State which parasite is depicted.
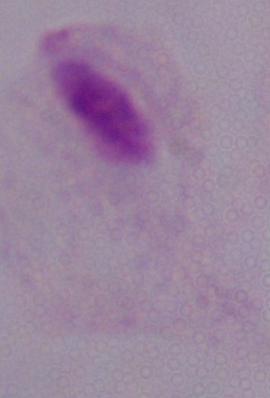

A trichomonad.

Summary:
  - Magnification: 1000x
  - Modality: photomicrograph